Locate every blood parasite and identify its species.
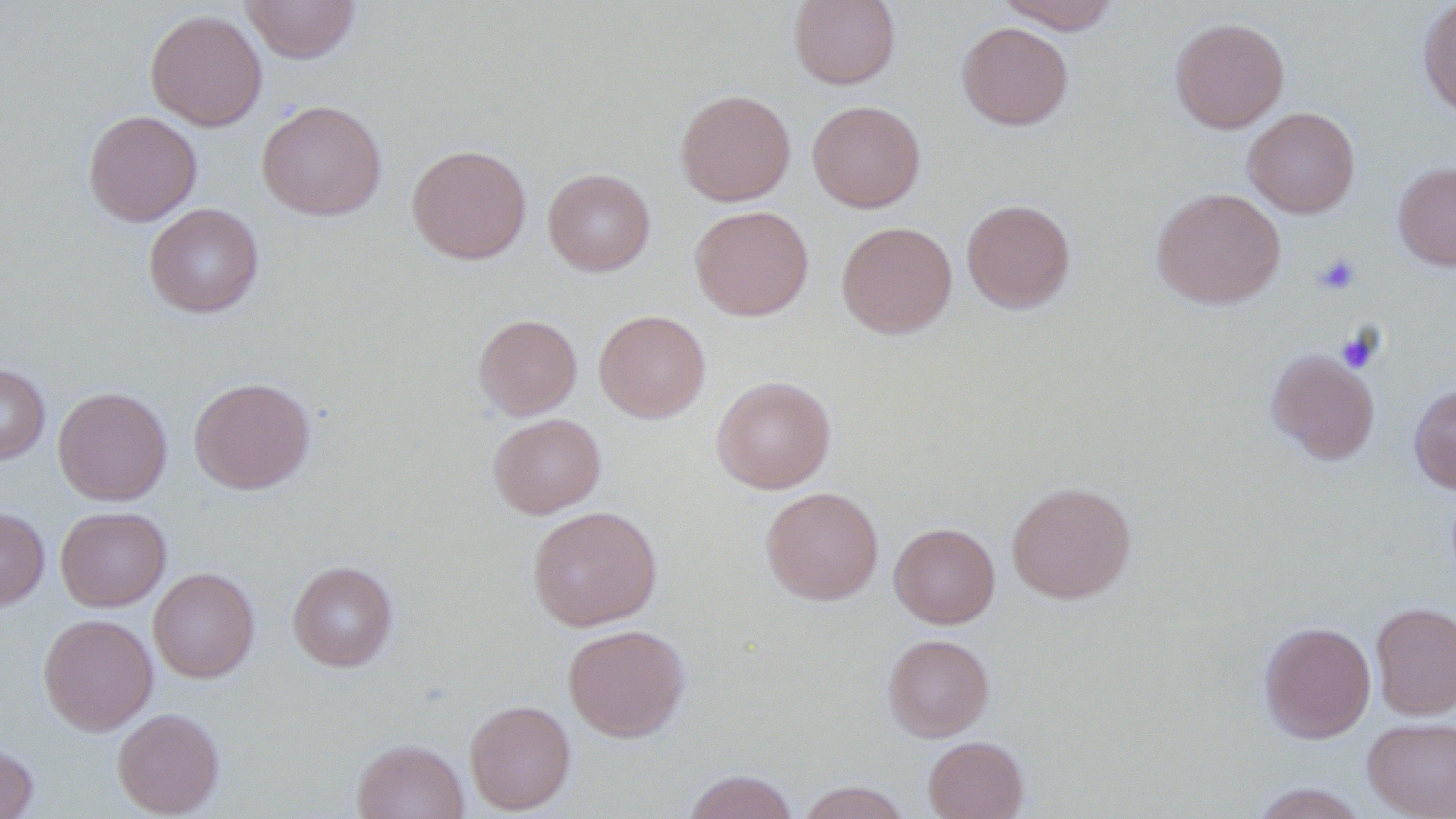
No blood parasites observed.

slide-level diagnosis = negative for blood parasites
modality = light microscopy
uninfected red blood cell locations = approximate bounding boxes as (x1, y1, x2, y2) in pixels: (241, 0, 361, 64), (789, 0, 900, 89), (995, 0, 1121, 33), (1417, 0, 1456, 120), (145, 9, 267, 131), (1170, 16, 1289, 133), (956, 22, 1073, 130), (676, 89, 795, 206), (257, 100, 386, 221), (807, 100, 925, 212), (1243, 106, 1360, 218), (83, 110, 202, 226), (406, 143, 531, 264), (1393, 162, 1456, 270), (543, 168, 655, 276), (1151, 187, 1286, 309), (961, 198, 1076, 313), (144, 203, 263, 318), (689, 205, 814, 321), (837, 221, 957, 338), (594, 309, 711, 423), (473, 314, 582, 420), (1266, 348, 1380, 464), (0, 363, 50, 464), (711, 375, 836, 494), (189, 376, 316, 494), (1408, 382, 1456, 494), (53, 386, 172, 505), (488, 413, 606, 518), (1006, 481, 1136, 603), (761, 486, 884, 605), (527, 505, 662, 631), (0, 506, 49, 611), (56, 506, 171, 611), (889, 523, 1000, 628), (287, 560, 398, 672), (149, 567, 259, 683), (1370, 601, 1456, 720), (39, 613, 158, 735), (1259, 621, 1376, 743), (563, 624, 690, 742), (882, 634, 994, 741), (464, 699, 575, 814), (112, 708, 225, 817), (1362, 716, 1456, 819), (923, 735, 1029, 819), (351, 738, 469, 819), (0, 742, 38, 819), (682, 769, 798, 819), (797, 780, 912, 819), (1246, 783, 1371, 818)
preparation = thin blood smear
platelet locations = approximate bounding boxes as (x1, y1, x2, y2) in pixels: (1314, 253, 1361, 296), (1336, 328, 1382, 374)
magnification = 1000x
image size = 1456×819 pixels
stain = May-Grünwald-Giemsa
field of view = single